Locate and identify every blood parasite.
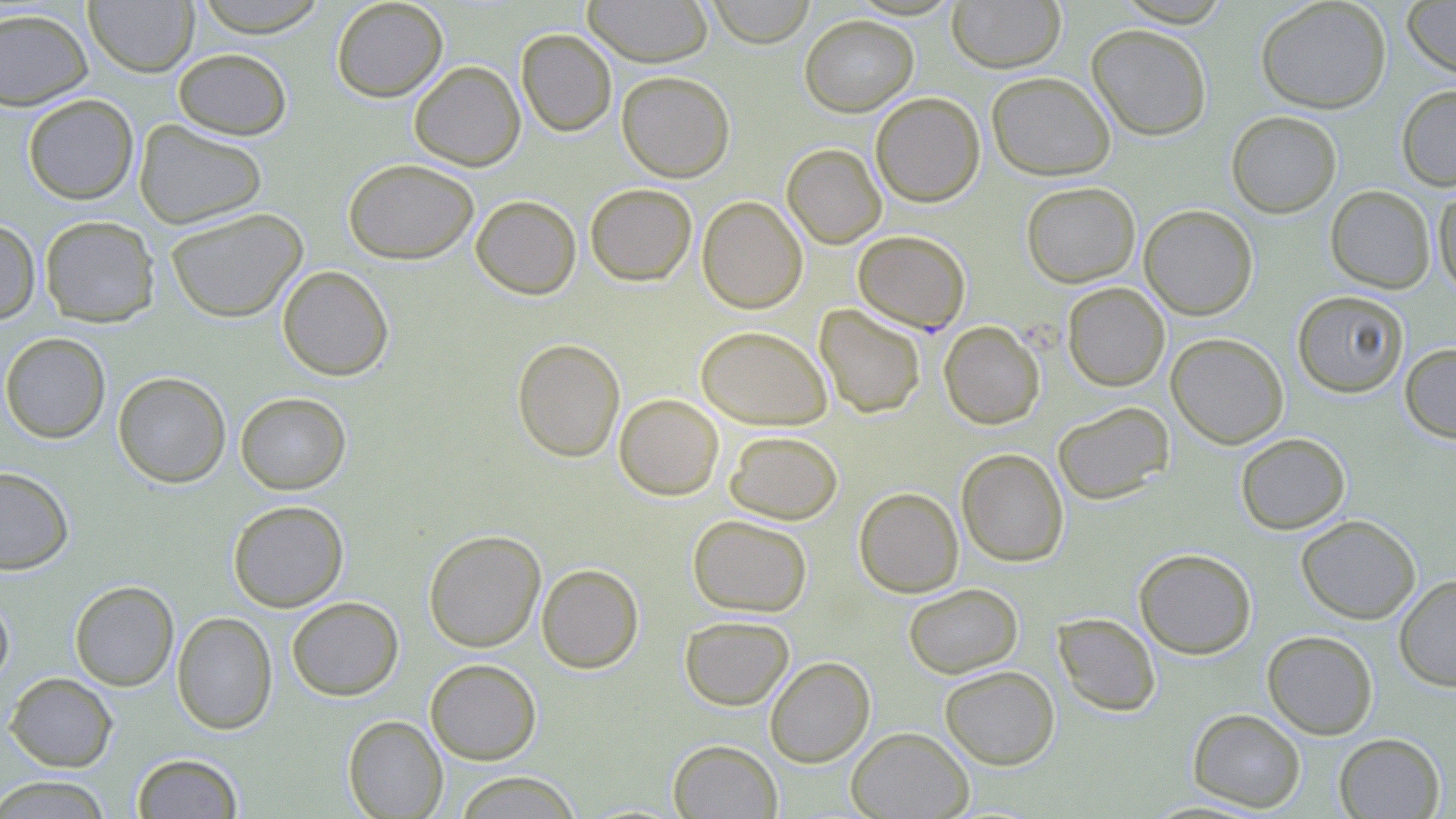

Approximate bounding boxes as (x1, y1, x2, y2) in pixels.
Plasmodium falciparum-infected red blood cells: (853, 230, 971, 334).
No Plasmodium ovale, Plasmodium malariae, Plasmodium vivax, Babesia divergens, or Trypanosoma brucei observed.

Uninfected red blood cell locations: (192, 0, 329, 37), (331, 0, 448, 102), (583, 0, 714, 67), (706, 0, 815, 48), (947, 0, 1066, 73), (1256, 0, 1391, 113), (1402, 0, 1456, 79), (83, 1, 199, 77), (0, 7, 94, 110), (799, 14, 919, 116), (1086, 23, 1212, 141), (516, 29, 617, 137), (172, 48, 292, 140), (408, 60, 525, 171), (617, 70, 735, 183), (986, 71, 1116, 181), (1396, 84, 1456, 191), (870, 92, 985, 207), (22, 93, 138, 205), (1226, 111, 1342, 218), (133, 119, 267, 230), (782, 143, 886, 249), (343, 158, 479, 265), (1021, 181, 1140, 288), (584, 183, 697, 286), (1432, 183, 1456, 297), (1325, 185, 1436, 293), (471, 195, 581, 300), (697, 196, 808, 314), (1139, 204, 1258, 320), (165, 207, 308, 323), (39, 215, 161, 327), (0, 219, 41, 324), (277, 265, 394, 381), (1062, 282, 1170, 391), (1292, 290, 1408, 397), (814, 304, 926, 418), (939, 321, 1045, 429), (695, 325, 832, 430), (0, 332, 111, 444), (1166, 332, 1288, 449), (512, 338, 625, 462), (1399, 343, 1456, 443), (113, 371, 231, 488), (235, 392, 352, 494), (614, 393, 724, 500), (1053, 401, 1174, 505), (724, 430, 843, 524), (1235, 432, 1351, 534), (956, 448, 1069, 567), (0, 466, 74, 575), (853, 487, 964, 598), (227, 500, 349, 612), (687, 514, 813, 617), (1296, 514, 1421, 624), (423, 529, 546, 652), (1134, 548, 1257, 659), (536, 563, 644, 673), (1394, 574, 1456, 691), (69, 580, 179, 691), (903, 583, 1023, 679), (0, 593, 14, 689), (287, 596, 403, 701), (171, 611, 278, 734), (1053, 612, 1161, 716), (680, 615, 794, 711), (1262, 630, 1378, 739), (765, 656, 875, 767), (425, 658, 542, 765), (939, 665, 1060, 769), (5, 672, 118, 772), (1188, 708, 1306, 812), (343, 715, 448, 818), (847, 726, 973, 818), (1333, 733, 1445, 818), (667, 739, 782, 818), (132, 753, 244, 818), (452, 771, 582, 818), (0, 775, 112, 818). Slide-level diagnosis: Plasmodium falciparum. Single field of view. May-Grünwald-Giemsa stain. Light microscopy. Captured at 1000x magnification. Thin blood film. Image is 1456×819 pixels.